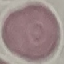

Summary:
  - Result: no malaria parasites detected
  - Image type: automatically extracted cell patch, resized to 64 × 64 pixels
  - Preparation: thin blood smear
  - Capture: smartphone camera at the microscope eyepiece
  - Stain: Giemsa